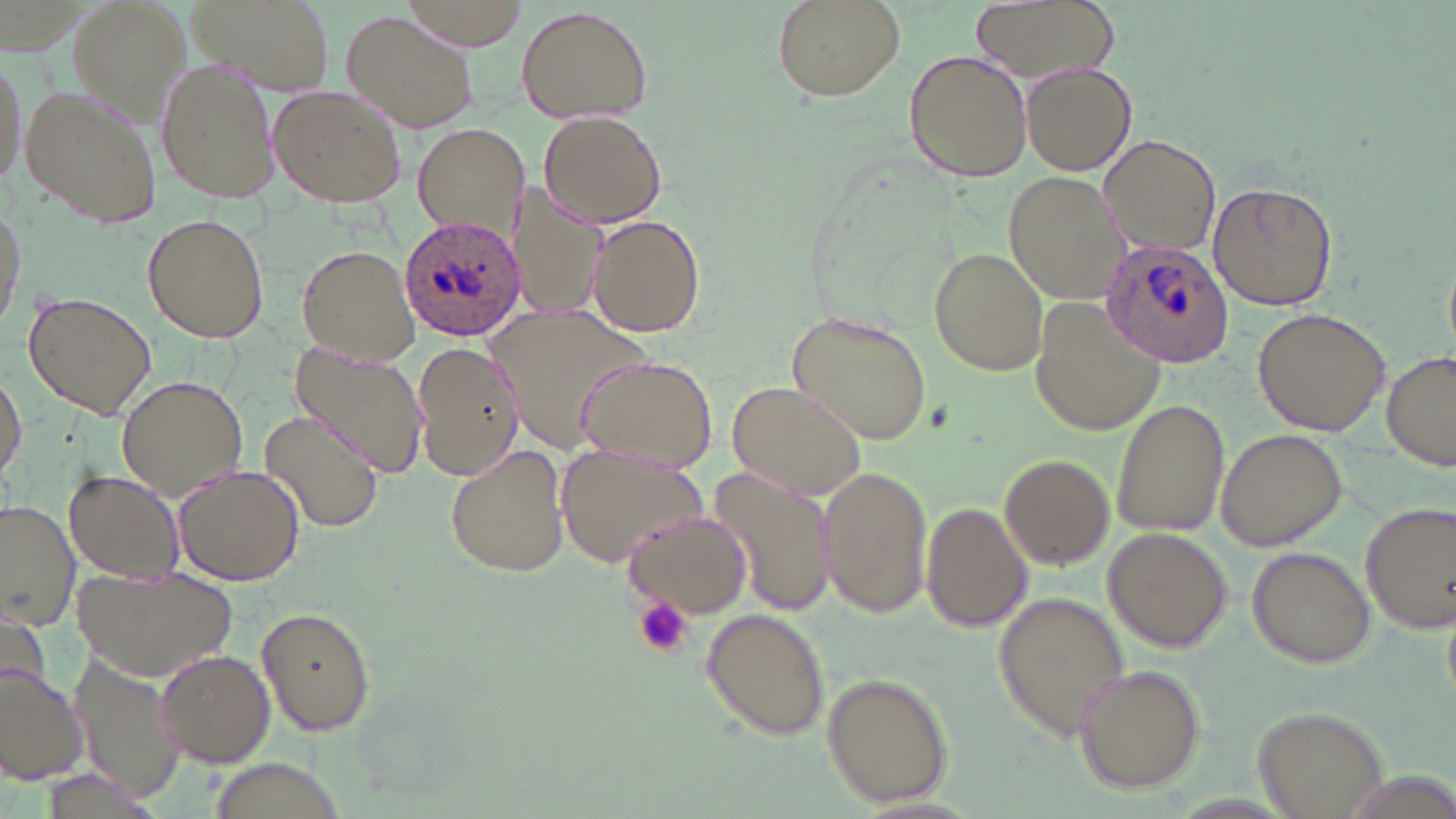

Summary:
  - Coordinate format: approximate bounding boxes as (x1,y1)-(x2,y2) corner pairs in pixels
  - Plasmodium ovale-infected red blood cell locations: (398,213)-(524,341), (1102,238)-(1234,368)
  - Uninfected red blood cell locations: (69,0)-(190,116), (185,0)-(338,94), (400,0)-(532,49), (772,0)-(903,102), (972,0)-(1119,82), (516,5)-(654,124), (342,10)-(475,132), (905,50)-(1033,182), (0,55)-(30,191), (157,56)-(280,205), (1023,62)-(1136,176), (19,84)-(161,230), (268,86)-(407,208), (538,110)-(667,229), (412,123)-(528,241), (1097,134)-(1222,259), (1004,173)-(1129,304), (510,181)-(610,323), (1208,182)-(1337,313), (0,194)-(27,334), (142,213)-(270,343), (586,214)-(707,336), (295,243)-(422,366), (928,246)-(1050,376), (21,290)-(156,421), (1028,296)-(1168,438), (482,300)-(658,459), (1251,307)-(1392,435), (786,310)-(932,445), (289,339)-(429,479), (412,340)-(525,481), (1384,349)-(1456,473), (576,353)-(717,473), (1,370)-(26,484), (117,375)-(249,500), (725,378)-(868,500), (1111,397)-(1230,540), (259,410)-(386,534), (1215,428)-(1348,550), (444,443)-(570,579), (557,443)-(708,570), (1000,452)-(1115,570), (171,462)-(304,586), (817,466)-(933,622), (708,467)-(836,619), (64,470)-(185,584), (0,500)-(79,628), (1360,500)-(1456,634), (921,501)-(1032,633), (622,509)-(754,620), (1102,528)-(1234,654), (1247,545)-(1375,668), (72,561)-(238,680), (994,591)-(1130,738), (255,606)-(377,738), (700,607)-(831,741), (154,648)-(277,767), (69,651)-(189,802), (0,662)-(92,786), (1071,663)-(1206,793), (820,671)-(954,809), (1253,703)-(1390,818)
  - Platelet locations: (635,598)-(694,659)
  - Slide-level diagnosis: Plasmodium ovale
  - Magnification: 1000x
  - Preparation: thin blood smear
  - Modality: light microscopy
  - Image size: 1456×819 pixels
  - Field of view: single
  - Stain: May-Grünwald-Giemsa